Locate every Plasmodium vivax-infected red blood cell.
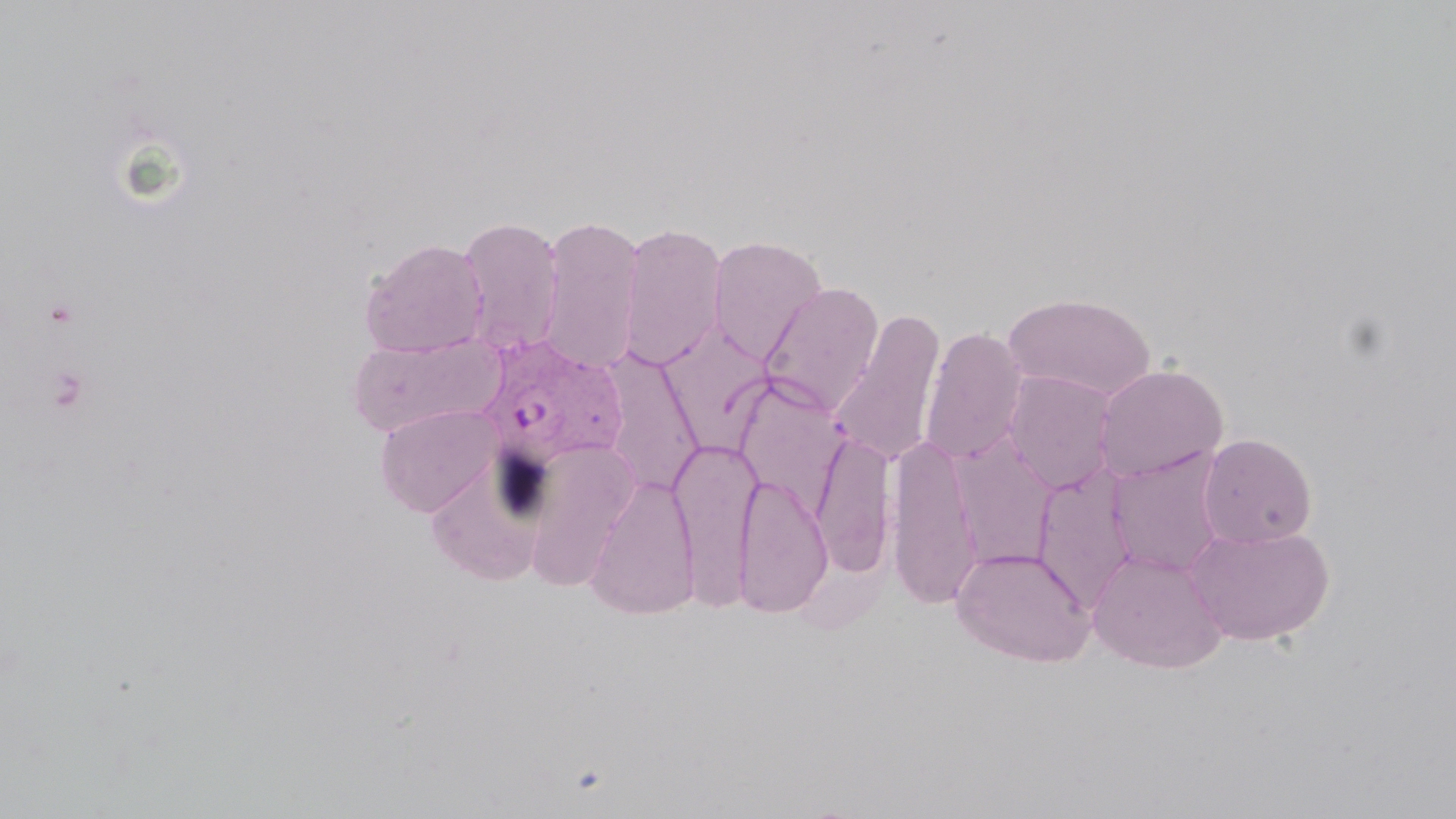

Approximate bounding boxes as (x1,y1)-(x2,y2) corner pairs in pixels.
Plasmodium vivax-infected red blood cells: (476,335)-(630,472).

slide_level_diagnosis: Plasmodium vivax
magnification: 1000x
stain: May-Grünwald-Giemsa
image_size: 1456×819 pixels
field_of_view: single
modality: optical microscopy
uninfected_red_blood_cell_locations: 'approximate bounding boxes as (x1,y1)-(x2,y2) corner pairs in pixels: (536,212)-(645,376), (457,214)-(565,357), (617,221)-(728,372), (708,235)-(829,364), (360,237)-(489,359), (759,282)-(884,417), (1003,292)-(1156,402), (830,309)-(946,467), (658,324)-(777,453), (919,325)-(1028,465), (346,331)-(507,437), (597,350)-(705,497), (1093,364)-(1229,483), (1003,370)-(1118,492), (732,376)-(852,515), (374,403)-(502,517), (812,431)-(895,575), (887,432)-(982,611), (1198,433)-(1317,548), (669,434)-(762,611), (520,437)-(640,592), (951,437)-(1058,572), (1106,448)-(1229,579), (1031,465)-(1138,611), (734,472)-(833,618), (585,473)-(701,620), (1185,523)-(1335,646), (951,545)-(1096,667), (1087,548)-(1229,673)'
preparation: thin blood film
platelet_locations: 'approximate bounding boxes as (x1,y1)-(x2,y2) corner pairs in pixels: (42,297)-(82,330), (45,364)-(92,415)'